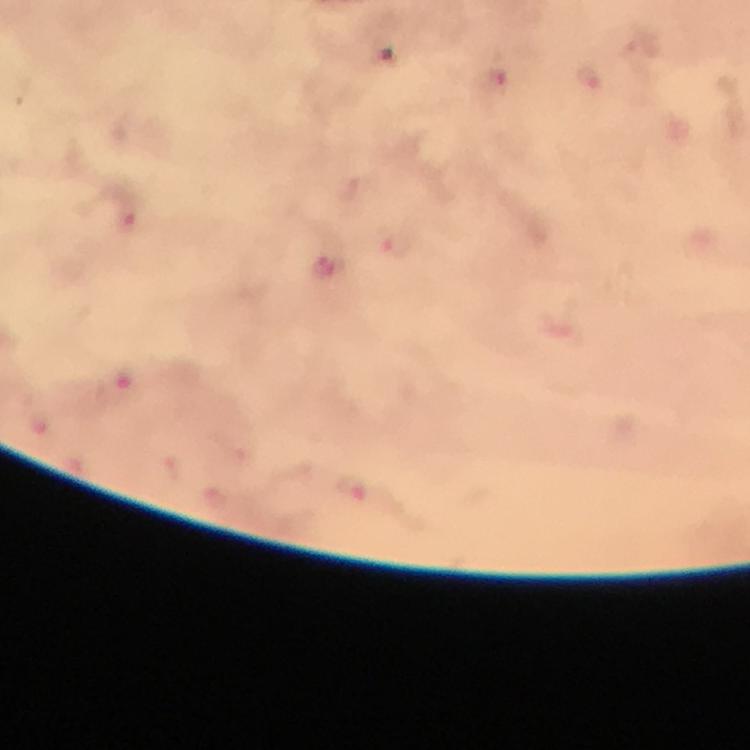 Approximate centers as {x, y} in pixels. Malaria parasite locations: {589, 76}, {497, 83}, {129, 213}, {396, 241}, {323, 264}, {117, 391}, {353, 486}. At 100x magnification. Image is 750×750 pixels. Photographed with a smartphone mounted on the microscope. Cropped region of a single field of view. Thick smear. From a malaria diagnostic workup. Giemsa-stained preparation. Immersion oil was used.